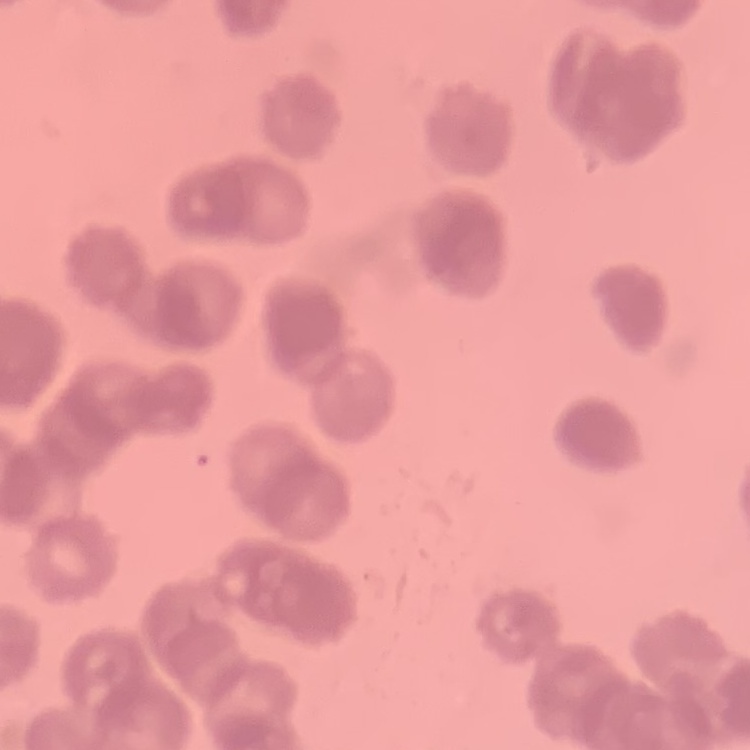 The erythrocytes show rouleaux formation. Field's or Giemsa stain. Thin peripheral smear. One tile cut from a larger photomicrograph.